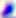
Toxoplasma gondii is seen. Captured at 400x magnification. Photomicrograph.